Name the parasite shown.
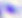

This is Toxoplasma gondii.

400x magnification. Micrograph.